Assess this cell for malaria.
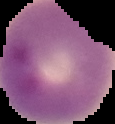
Parasitized.

Summary:
  - Image size: 115×124 pixels
  - Image type: segmented cell region on a black background
  - Preparation: thin blood film